Identify the parasite.
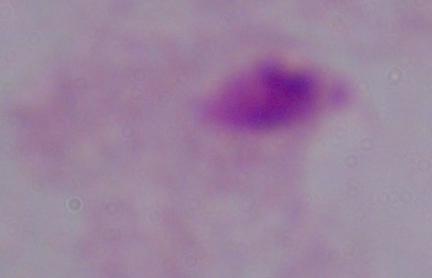

This is a trichomonad.

Summary:
  - Magnification: 1000x
  - Modality: micrograph